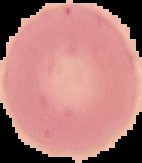

From a thin blood smear. Segmented cell region on a black background. Image is 142×163 pixels. Result: negative for malaria parasites.